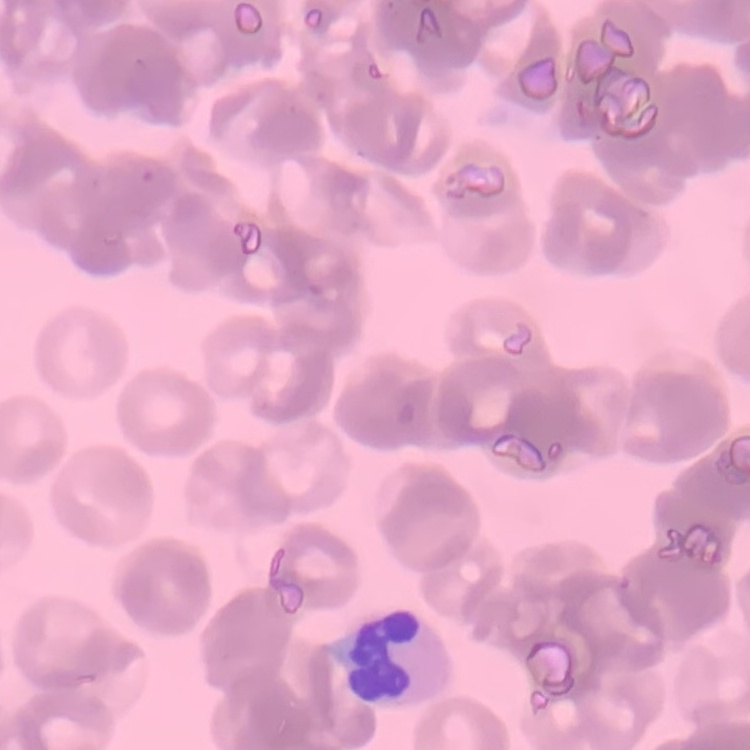

Summary:
  - Red blood cell morphology: rouleaux formation
  - Stain: Field's or Giemsa
  - Image type: square crop of a larger photomicrograph
  - Preparation: thin peripheral smear